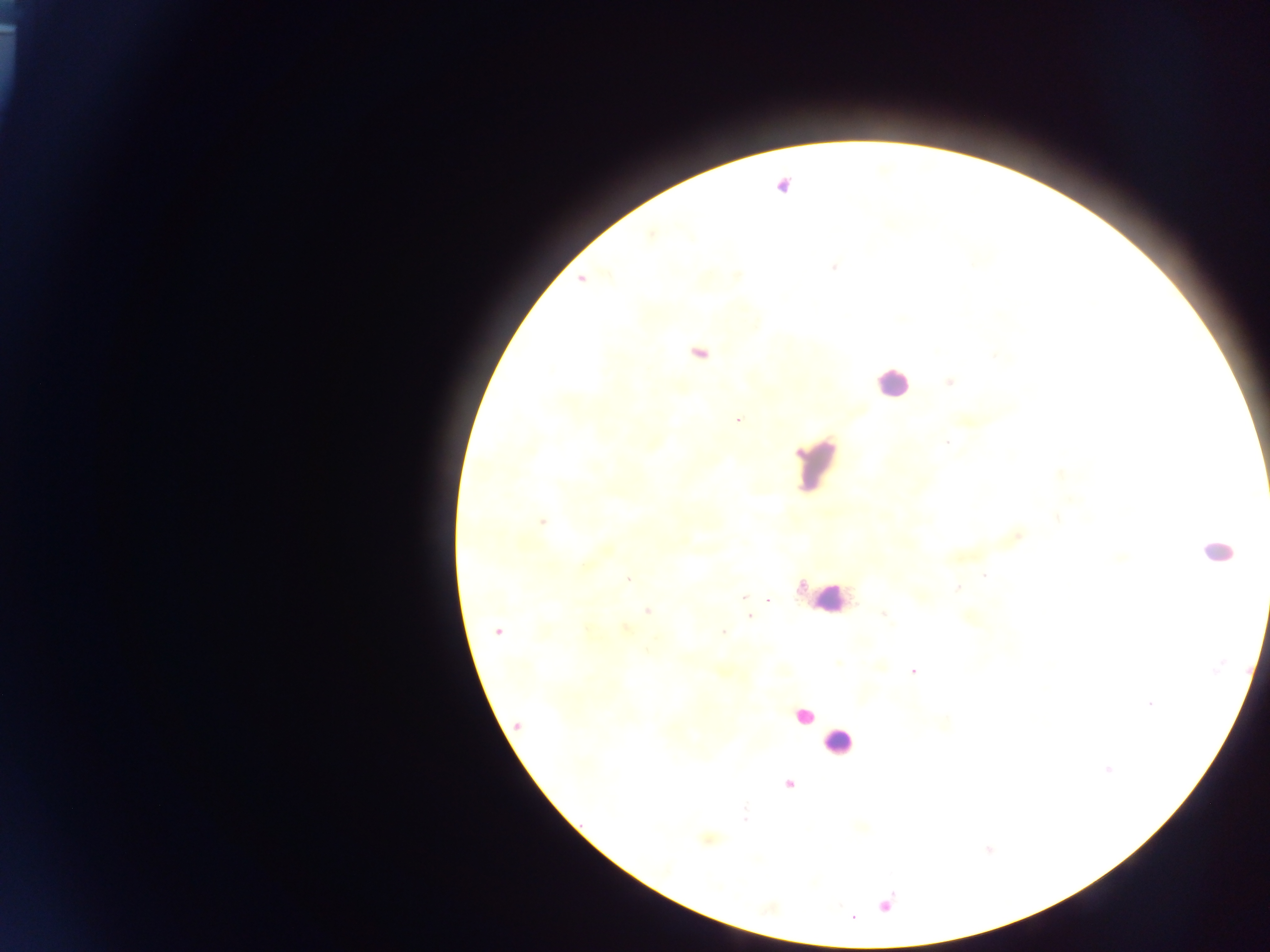

Approximate centers as (x, y) in pixels.
Summary:
  - Leukocyte locations: (891, 383), (819, 465), (1216, 551), (830, 598), (805, 716), (837, 742)
  - Plasmodium parasite locations: (784, 185), (834, 268), (581, 279), (699, 353), (950, 382), (738, 420), (949, 443), (1058, 475), (1057, 518), (543, 522), (1122, 556), (984, 576), (629, 578), (958, 587), (745, 596), (769, 600), (648, 611), (883, 614), (750, 617), (497, 631), (724, 632), (913, 671), (1149, 704), (518, 724), (1108, 769), (789, 785), (745, 814), (884, 905)
  - Country: Ghana
  - Preparation: thick blood film
  - Image size: 1270×952 pixels
  - Field of view: single
  - Capture: mobile-phone photograph through a microscope